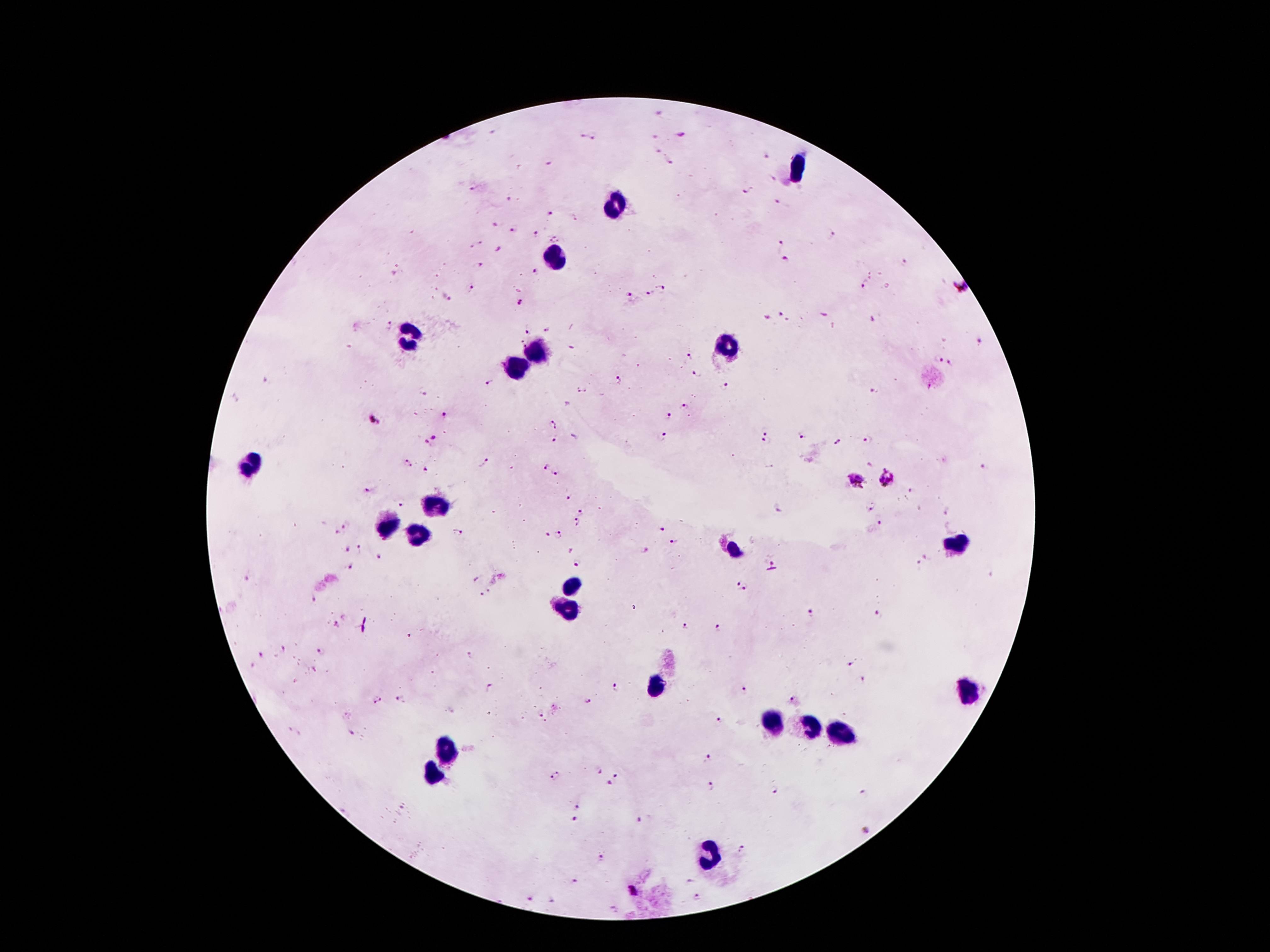
Approximate centers as [x, y] in pixels.
Summary:
  - Leukocyte locations: [796, 166], [615, 203], [553, 256], [407, 334], [728, 345], [540, 347], [518, 365], [250, 464], [433, 504], [389, 524], [416, 535], [955, 542], [734, 550], [573, 586], [568, 603], [655, 685], [969, 690], [772, 721], [807, 729], [840, 732], [445, 749], [431, 776], [712, 853]
  - Malaria parasite locations: [680, 135], [582, 136], [594, 136], [655, 152], [766, 155], [548, 162], [669, 163], [772, 180], [471, 190], [747, 192], [507, 198], [779, 202], [550, 216], [493, 226], [513, 231], [536, 233], [830, 233], [555, 238], [477, 243], [779, 246], [499, 248], [783, 259], [904, 262], [480, 264], [534, 270], [865, 284], [662, 288], [962, 288], [470, 289], [651, 294], [633, 295], [445, 297], [521, 303], [782, 314], [766, 318], [388, 325], [548, 328], [526, 331], [980, 341], [521, 342], [689, 356], [938, 357], [950, 362], [697, 373], [618, 378], [489, 381], [726, 385], [581, 390], [874, 390], [422, 394], [683, 406], [444, 415], [668, 415], [373, 419], [551, 424], [764, 430], [801, 436], [434, 437], [662, 437], [554, 440], [766, 440], [837, 441], [868, 441], [426, 442], [482, 460], [406, 464], [546, 466], [984, 467], [425, 469], [555, 473], [887, 479], [855, 481], [366, 490], [914, 491], [569, 497], [401, 502], [871, 507], [581, 511], [345, 523], [576, 523], [880, 523], [662, 527], [336, 532], [458, 533], [548, 535], [560, 535], [675, 541], [348, 548], [360, 548], [570, 550], [644, 550], [927, 556], [379, 557], [773, 562], [576, 563], [919, 563], [349, 564], [474, 580], [738, 584], [744, 588], [488, 590], [481, 594], [314, 600], [808, 611], [880, 613], [335, 626], [685, 626], [717, 628], [285, 647], [322, 651], [260, 655], [852, 664], [864, 680], [487, 688], [615, 688], [742, 689], [379, 699], [399, 699], [588, 701], [792, 701], [538, 712], [717, 720], [350, 731], [707, 758], [600, 770], [556, 775], [614, 776], [611, 783], [711, 787], [777, 791], [861, 792], [578, 806], [402, 808], [575, 820], [639, 821], [868, 830], [742, 849], [600, 854], [573, 880], [691, 882], [633, 891], [529, 898], [697, 898], [554, 900]
  - Patient malaria status: positive for Plasmodium falciparum
  - Image size: 1270×952 pixels
  - Field of view: one from this slide
  - Preparation: thick peripheral-blood smear
  - Stain: Giemsa
  - Capture: smartphone camera through the microscope eyepiece
  - Magnification: 100x